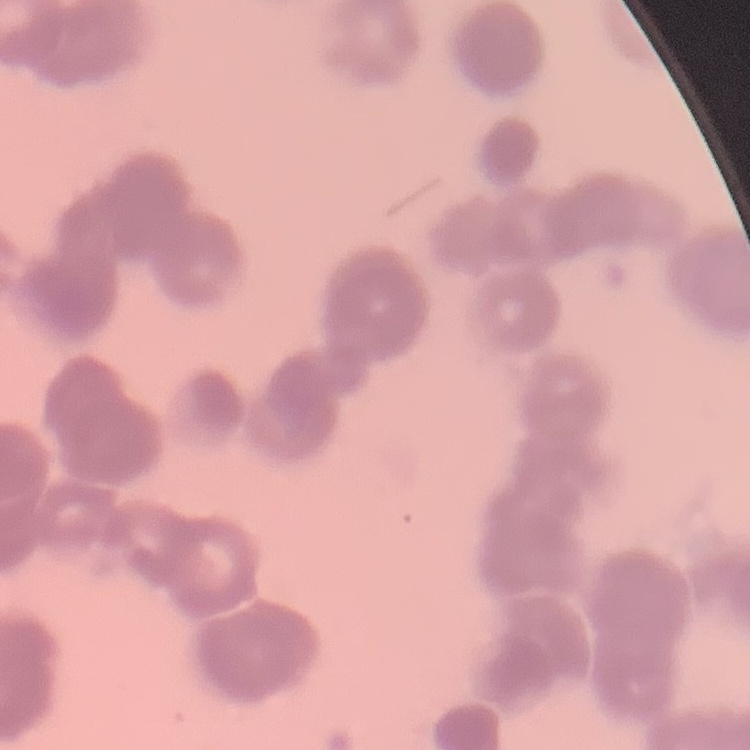
red blood cell morphology = rouleaux formation
stain = Field's or Giemsa
preparation = thin blood smear
image type = square crop of a larger photomicrograph